Report the malaria status of this cell.
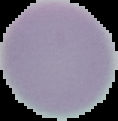
It is uninfected.

Image is 118×121 pixels. The area outside the segmented cell region is set to black. From a thin blood film.